State the blood parasite species.
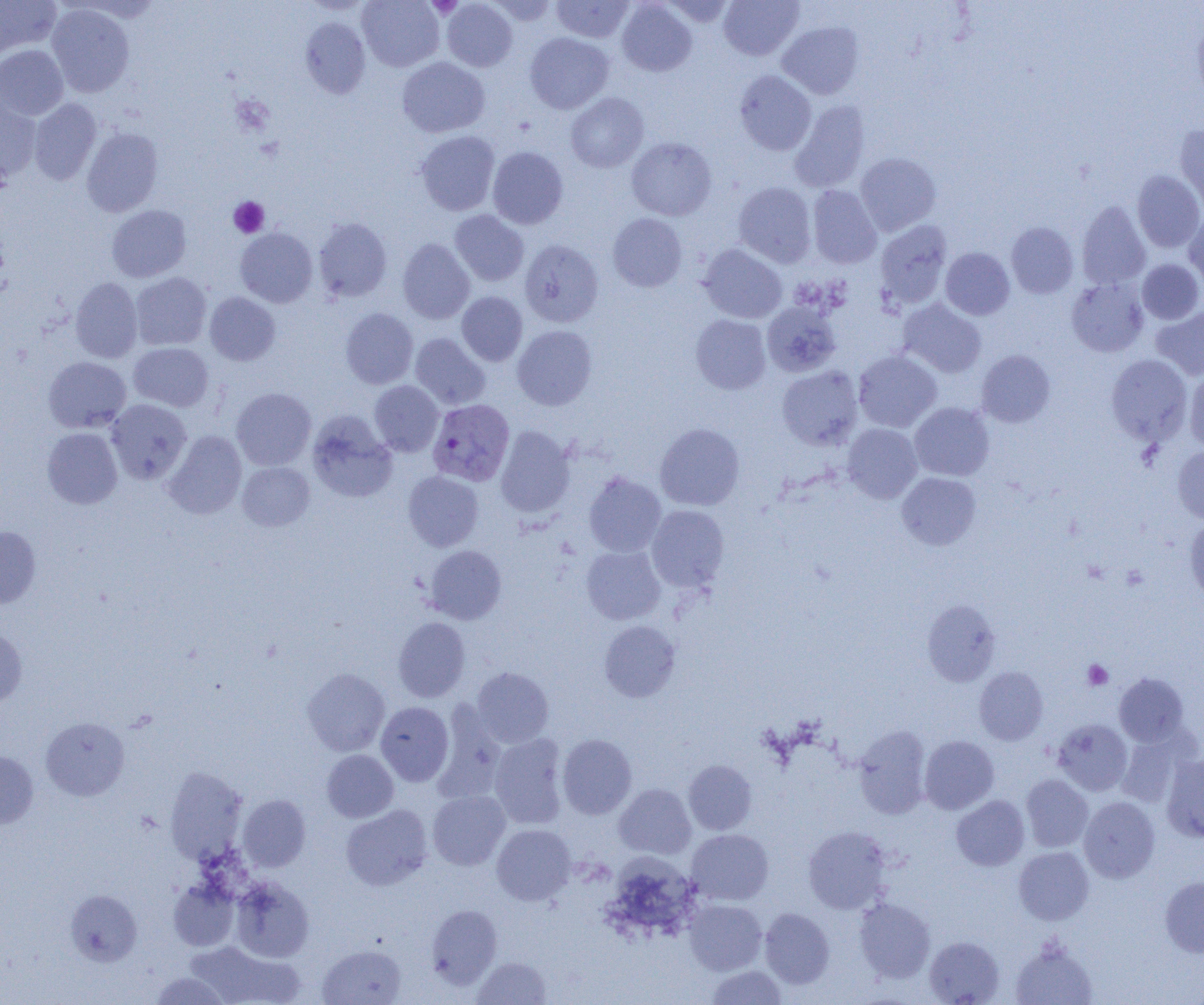

Plasmodium vivax.

{
  "uninfected_red_blood_cell_locations": "approximate bounding boxes as named x1/y1/x2/y2 corners in pixels: (x1=0, y1=0, x2=61, y2=57), (x1=357, y1=0, x2=444, y2=71), (x1=485, y1=0, x2=557, y2=25), (x1=551, y1=0, x2=634, y2=43), (x1=661, y1=0, x2=736, y2=27), (x1=719, y1=0, x2=803, y2=61), (x1=441, y1=1, x2=517, y2=71), (x1=616, y1=1, x2=697, y2=76), (x1=47, y1=4, x2=135, y2=97), (x1=1193, y1=14, x2=1204, y2=105), (x1=300, y1=16, x2=371, y2=99), (x1=777, y1=21, x2=864, y2=99), (x1=525, y1=32, x2=614, y2=114), (x1=0, y1=45, x2=68, y2=120), (x1=397, y1=57, x2=490, y2=137), (x1=734, y1=70, x2=816, y2=155), (x1=565, y1=92, x2=649, y2=172), (x1=0, y1=93, x2=42, y2=183), (x1=28, y1=98, x2=102, y2=185), (x1=790, y1=100, x2=870, y2=192), (x1=1175, y1=125, x2=1204, y2=212), (x1=82, y1=127, x2=163, y2=217), (x1=416, y1=131, x2=500, y2=215), (x1=626, y1=137, x2=717, y2=220), (x1=487, y1=147, x2=568, y2=229), (x1=855, y1=152, x2=940, y2=235), (x1=1132, y1=170, x2=1204, y2=253), (x1=733, y1=182, x2=816, y2=267), (x1=807, y1=185, x2=882, y2=269), (x1=1077, y1=200, x2=1151, y2=289), (x1=107, y1=205, x2=191, y2=282), (x1=449, y1=210, x2=529, y2=286), (x1=1184, y1=211, x2=1204, y2=288), (x1=607, y1=213, x2=687, y2=292), (x1=313, y1=217, x2=392, y2=302), (x1=875, y1=220, x2=952, y2=309), (x1=1006, y1=222, x2=1078, y2=298), (x1=235, y1=228, x2=318, y2=308), (x1=397, y1=238, x2=474, y2=324), (x1=520, y1=239, x2=604, y2=327), (x1=698, y1=244, x2=787, y2=323), (x1=940, y1=247, x2=1014, y2=320), (x1=1138, y1=259, x2=1204, y2=324), (x1=130, y1=272, x2=211, y2=350), (x1=70, y1=277, x2=142, y2=363), (x1=1066, y1=279, x2=1148, y2=357), (x1=205, y1=292, x2=280, y2=366), (x1=456, y1=292, x2=527, y2=366), (x1=898, y1=299, x2=986, y2=378), (x1=762, y1=301, x2=841, y2=377), (x1=1151, y1=306, x2=1204, y2=381), (x1=340, y1=308, x2=419, y2=389), (x1=690, y1=314, x2=771, y2=394), (x1=513, y1=325, x2=597, y2=410), (x1=410, y1=333, x2=490, y2=410), (x1=129, y1=342, x2=213, y2=412), (x1=853, y1=350, x2=942, y2=432), (x1=977, y1=350, x2=1055, y2=427), (x1=1106, y1=354, x2=1192, y2=445), (x1=43, y1=357, x2=131, y2=432), (x1=777, y1=366, x2=863, y2=449), (x1=1184, y1=370, x2=1204, y2=453), (x1=369, y1=380, x2=444, y2=456), (x1=231, y1=387, x2=316, y2=470), (x1=106, y1=399, x2=191, y2=484), (x1=909, y1=402, x2=994, y2=481), (x1=307, y1=412, x2=397, y2=503), (x1=655, y1=423, x2=745, y2=510), (x1=842, y1=424, x2=922, y2=503), (x1=495, y1=426, x2=575, y2=517), (x1=42, y1=427, x2=122, y2=509), (x1=164, y1=431, x2=247, y2=519), (x1=1173, y1=446, x2=1204, y2=524), (x1=237, y1=461, x2=315, y2=531), (x1=403, y1=471, x2=484, y2=551), (x1=584, y1=472, x2=666, y2=557), (x1=897, y1=472, x2=981, y2=550), (x1=646, y1=505, x2=729, y2=592), (x1=1184, y1=519, x2=1204, y2=601), (x1=0, y1=526, x2=41, y2=607), (x1=424, y1=545, x2=507, y2=624), (x1=581, y1=545, x2=665, y2=625), (x1=922, y1=600, x2=1000, y2=685), (x1=393, y1=617, x2=471, y2=702), (x1=599, y1=621, x2=680, y2=702), (x1=0, y1=624, x2=27, y2=708), (x1=974, y1=666, x2=1048, y2=745), (x1=472, y1=667, x2=553, y2=747), (x1=302, y1=668, x2=390, y2=755), (x1=1114, y1=673, x2=1188, y2=746), (x1=375, y1=701, x2=454, y2=786), (x1=433, y1=703, x2=506, y2=803), (x1=40, y1=717, x2=129, y2=800), (x1=1052, y1=719, x2=1132, y2=795), (x1=853, y1=726, x2=932, y2=818), (x1=1116, y1=732, x2=1189, y2=807), (x1=489, y1=734, x2=568, y2=828), (x1=557, y1=734, x2=637, y2=819), (x1=919, y1=735, x2=999, y2=814), (x1=322, y1=750, x2=398, y2=822), (x1=0, y1=751, x2=38, y2=829), (x1=1162, y1=754, x2=1204, y2=843), (x1=683, y1=760, x2=756, y2=835), (x1=165, y1=767, x2=249, y2=865), (x1=1021, y1=774, x2=1093, y2=852), (x1=614, y1=783, x2=696, y2=859), (x1=427, y1=790, x2=510, y2=870), (x1=238, y1=794, x2=311, y2=871), (x1=951, y1=795, x2=1029, y2=870), (x1=1078, y1=796, x2=1160, y2=883), (x1=341, y1=804, x2=433, y2=891), (x1=492, y1=824, x2=576, y2=905), (x1=803, y1=826, x2=892, y2=914), (x1=686, y1=829, x2=774, y2=905), (x1=1013, y1=846, x2=1093, y2=925), (x1=605, y1=854, x2=699, y2=940), (x1=1160, y1=876, x2=1204, y2=957), (x1=230, y1=877, x2=314, y2=962), (x1=168, y1=878, x2=240, y2=951), (x1=65, y1=890, x2=141, y2=966), (x1=854, y1=898, x2=935, y2=983), (x1=684, y1=899, x2=767, y2=974), (x1=426, y1=904, x2=501, y2=988), (x1=760, y1=908, x2=835, y2=988), (x1=924, y1=936, x2=1004, y2=1004), (x1=1010, y1=937, x2=1099, y2=1005), (x1=184, y1=940, x2=304, y2=1005), (x1=318, y1=944, x2=406, y2=1004), (x1=471, y1=956, x2=552, y2=1004), (x1=705, y1=965, x2=788, y2=1004), (x1=150, y1=972, x2=232, y2=1005)",
  "magnification": "1000x",
  "preparation": "thin blood smear",
  "platelet_locations": "approximate bounding boxes as named x1/y1/x2/y2 corners in pixels: (x1=428, y1=0, x2=462, y2=18), (x1=228, y1=197, x2=269, y2=237), (x1=1082, y1=659, x2=1113, y2=691)",
  "modality": "optical microscopy",
  "image_size": "1204×1005 pixels",
  "field_of_view": "one of a larger specimen",
  "plasmodium_vivax_infected_red_blood_cell_locations": "approximate bounding boxes as named x1/y1/x2/y2 corners in pixels: (x1=427, y1=398, x2=515, y2=486)"
}